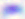
modality = photomicrograph
identification = Toxoplasma gondii
magnification = 400x